Report the malaria status of this cell.
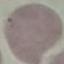
Uninfected.

Automatically extracted cell patch, resized to 64 × 64 pixels. Giemsa stain. Acquired by smartphone through the microscope eyepiece. Thin smear of blood.